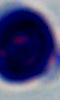 A leukocyte is shown. Photomicrograph. 1000x magnification.